Locate every blood parasite and identify its species.
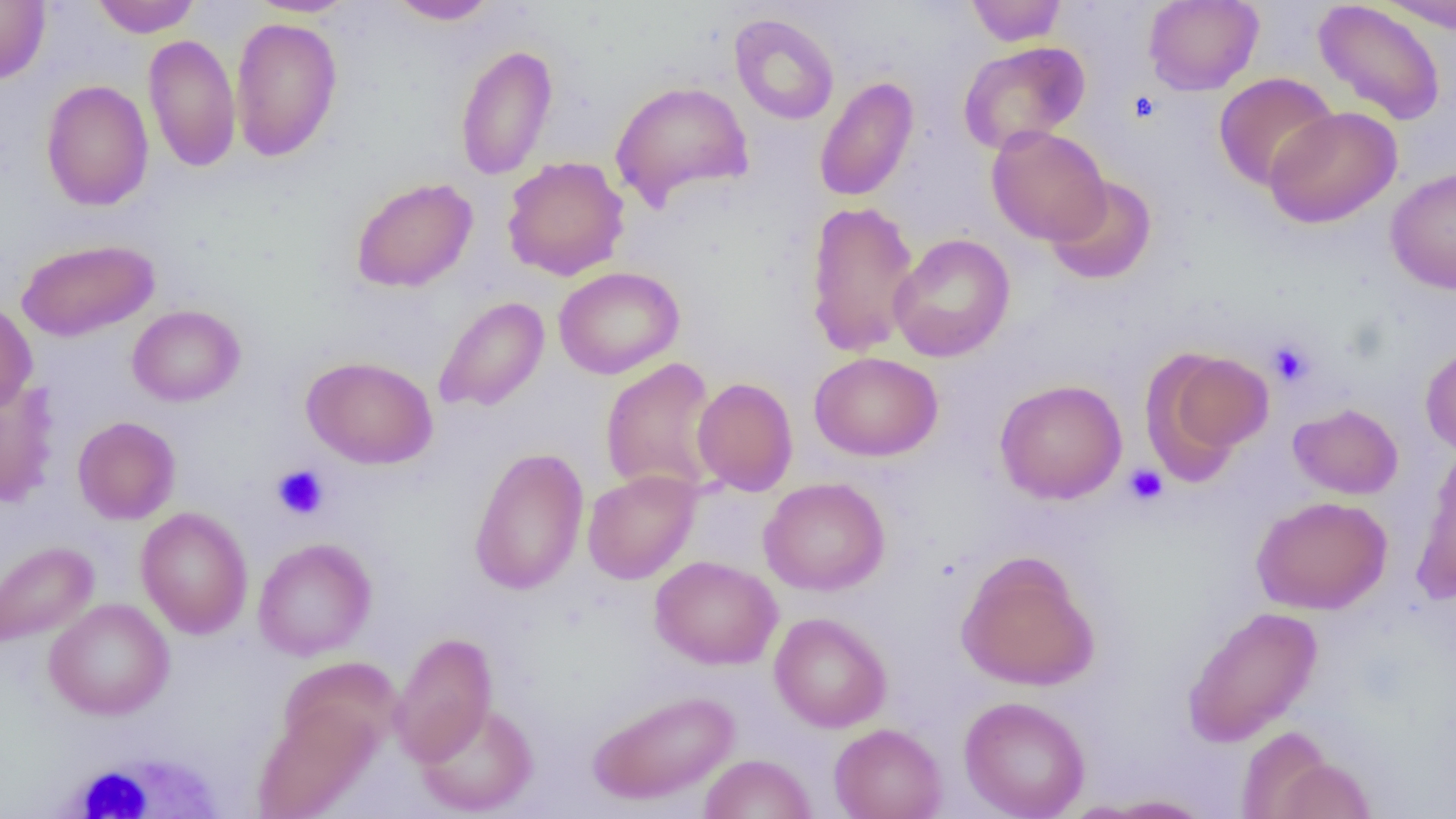
No blood parasites seen.

Approximate bounding boxes as [x1, y1, x2, y2] in pixels. Platelet locations: [1128, 90, 1162, 123], [1266, 338, 1314, 387], [272, 464, 329, 520], [1123, 464, 1168, 506]. White blood cell locations: [45, 745, 233, 819]. Uninfected red blood cell locations: [91, 0, 200, 37], [247, 0, 359, 17], [386, 0, 500, 25], [966, 0, 1067, 46], [1143, 0, 1264, 95], [1377, 0, 1456, 33], [0, 1, 51, 83], [1313, 1, 1447, 126], [729, 13, 839, 125], [229, 16, 343, 162], [143, 33, 241, 173], [957, 40, 1090, 154], [455, 43, 558, 181], [1213, 72, 1339, 191], [814, 76, 919, 203], [41, 80, 154, 211], [610, 80, 754, 210], [1263, 106, 1402, 229], [986, 125, 1111, 246], [502, 156, 630, 281], [1386, 167, 1456, 294], [1044, 175, 1158, 286], [351, 177, 478, 293], [804, 200, 921, 357], [888, 233, 1015, 362], [16, 238, 160, 342], [554, 266, 684, 379], [433, 296, 549, 412], [0, 301, 37, 415], [127, 304, 245, 407], [1420, 343, 1456, 456], [1145, 346, 1274, 473], [809, 351, 943, 461], [301, 355, 438, 469], [600, 357, 720, 498], [692, 377, 798, 496], [994, 379, 1127, 504], [0, 380, 60, 508], [1288, 402, 1403, 499], [72, 416, 180, 524], [469, 446, 589, 595], [1412, 446, 1456, 604], [582, 469, 701, 584], [758, 477, 890, 596], [1251, 495, 1392, 615], [135, 506, 253, 639], [253, 538, 376, 661], [0, 540, 99, 648], [956, 551, 1100, 691], [650, 555, 782, 669], [44, 598, 174, 720], [1183, 605, 1323, 747], [769, 612, 891, 732], [391, 632, 498, 766], [278, 657, 402, 762], [587, 689, 740, 806], [959, 695, 1090, 819], [417, 702, 538, 816], [252, 705, 379, 819], [829, 723, 947, 819], [1237, 725, 1336, 818], [700, 753, 817, 819], [1271, 756, 1376, 818], [1094, 794, 1216, 817]. Slide-level diagnosis: negative for blood parasites. Thin blood smear. Image is 1456×819 pixels. One field of a larger specimen. Light microscopy. 1000x magnification.